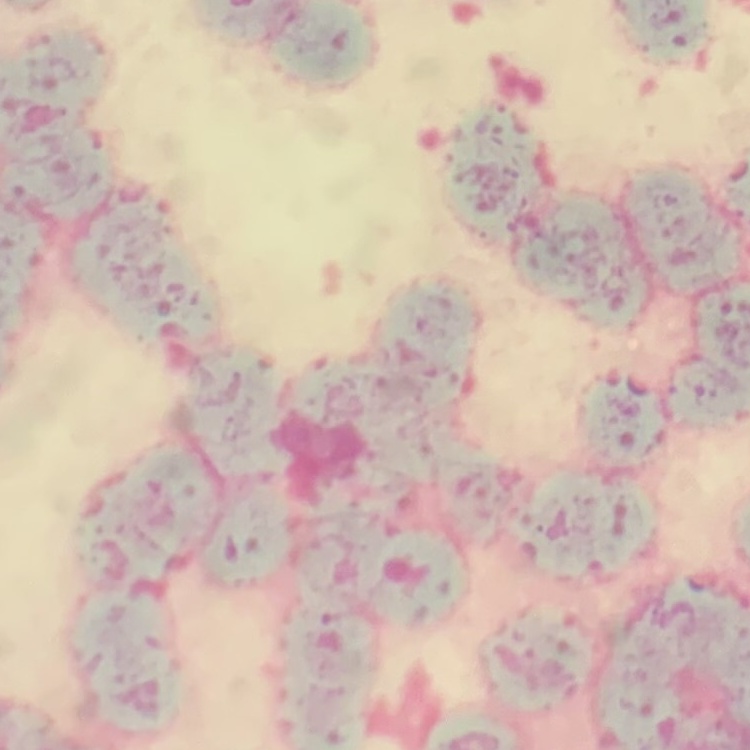

erythrocyte_morphology: rouleaux formation
image_type: one tile cut from a larger photomicrograph
stain: Field's or Giemsa
preparation: thin blood film